Report the malaria status of this cell.
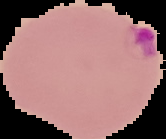
Parasitized.

Summary:
  - Preparation: thin blood film
  - Image size: 166×139 pixels
  - Image type: cell region segmented out of the field of view; surrounding area masked to black